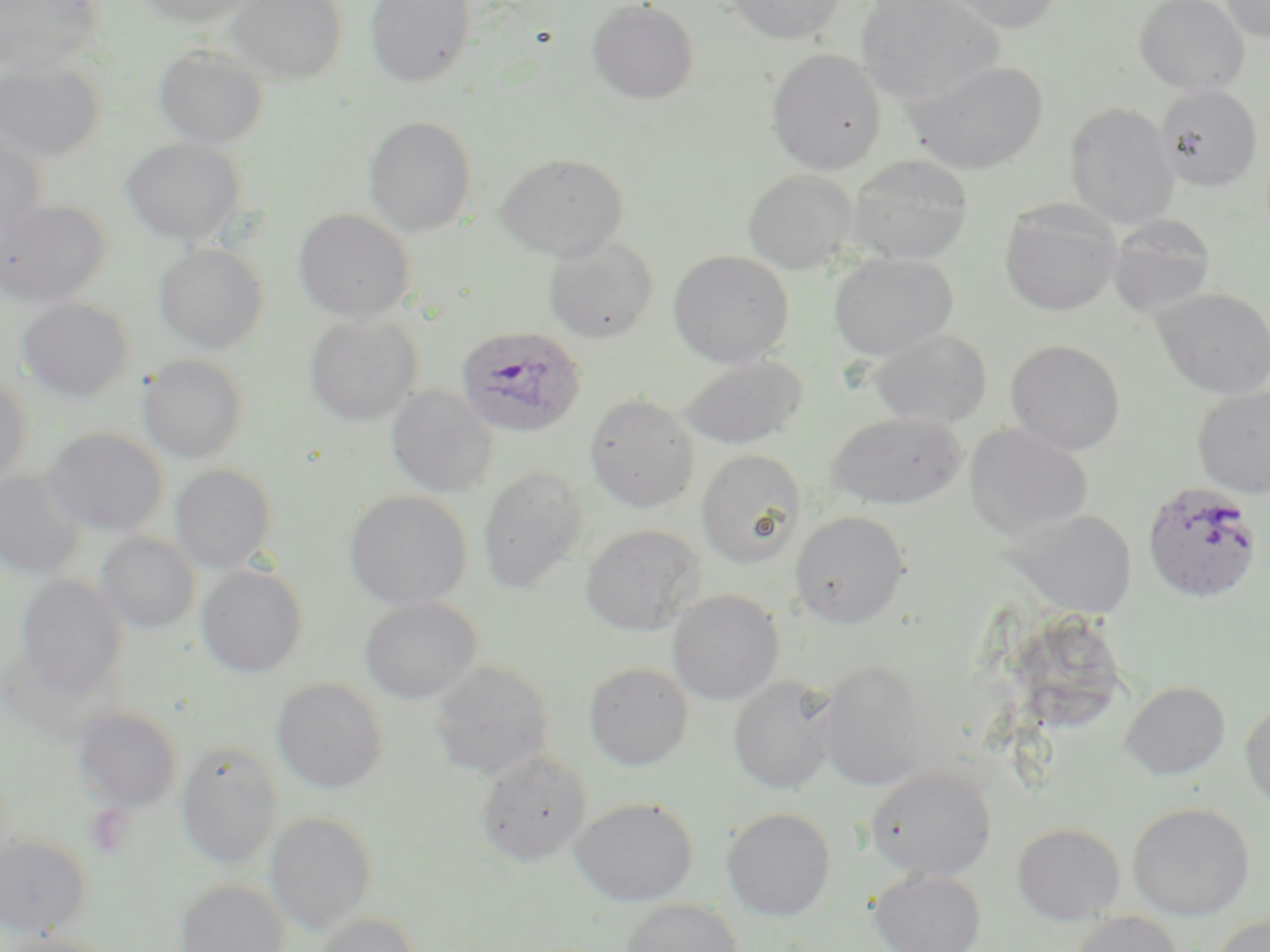

Summary:
  - Coordinate format: approximate bounding boxes as (x1,y1)-(x2,y2) corner pairs in pixels
  - Plasmodium ovale-infected red blood cell locations: (454,325)-(586,438), (1141,481)-(1263,604)
  - Uninfected red blood cell locations: (0,0)-(103,76), (135,0)-(258,28), (227,0)-(348,84), (364,0)-(476,88), (722,0)-(848,45), (856,0)-(1005,107), (931,0)-(1063,34), (1134,0)-(1250,96), (1220,0)-(1270,43), (586,1)-(699,105), (153,44)-(269,151), (766,48)-(887,175), (0,57)-(105,164), (905,59)-(1049,175), (1155,84)-(1264,192), (1064,102)-(1180,229), (363,116)-(477,237), (0,130)-(48,241), (122,138)-(245,244), (495,153)-(629,261), (847,154)-(974,265), (743,169)-(858,274), (0,198)-(110,307), (999,200)-(1123,317), (293,209)-(415,323), (1107,214)-(1217,318), (543,236)-(659,344), (154,243)-(269,353), (668,250)-(794,368), (828,253)-(958,361), (1151,287)-(1270,399), (16,299)-(134,402), (304,315)-(422,426), (867,328)-(992,429), (1006,339)-(1126,455), (138,354)-(248,463), (677,355)-(808,450), (0,375)-(31,489), (386,385)-(497,496), (1192,386)-(1270,498), (583,393)-(700,512), (826,412)-(968,509), (963,423)-(1094,544), (41,427)-(169,537), (696,449)-(807,568), (169,465)-(278,573), (477,466)-(588,594), (0,469)-(86,581), (343,491)-(473,610), (1004,507)-(1138,618), (790,510)-(910,629), (581,524)-(705,636), (96,532)-(200,633), (195,564)-(308,677), (15,575)-(128,696), (667,590)-(784,705), (359,596)-(481,704), (815,659)-(927,792), (428,660)-(554,780), (583,662)-(694,771), (728,676)-(841,794), (271,678)-(388,794), (1120,681)-(1230,780), (1240,697)-(1270,813), (72,706)-(182,812), (175,740)-(283,869), (475,749)-(592,867), (864,766)-(997,881), (570,796)-(698,906), (1127,802)-(1255,921), (722,806)-(836,921), (264,811)-(378,935), (1012,823)-(1126,926), (0,835)-(92,935), (869,869)-(986,952), (174,879)-(290,952), (618,899)-(744,952), (1067,911)-(1184,952), (313,912)-(423,952), (1209,913)-(1269,952), (2,932)-(116,952)
  - Slide-level diagnosis: Plasmodium ovale
  - Preparation: thin blood smear
  - Stain: May-Grünwald-Giemsa
  - Image size: 1270×952 pixels
  - Modality: light microscopy
  - Magnification: 1000x
  - Field of view: single